Find each parasitized red blood cell.
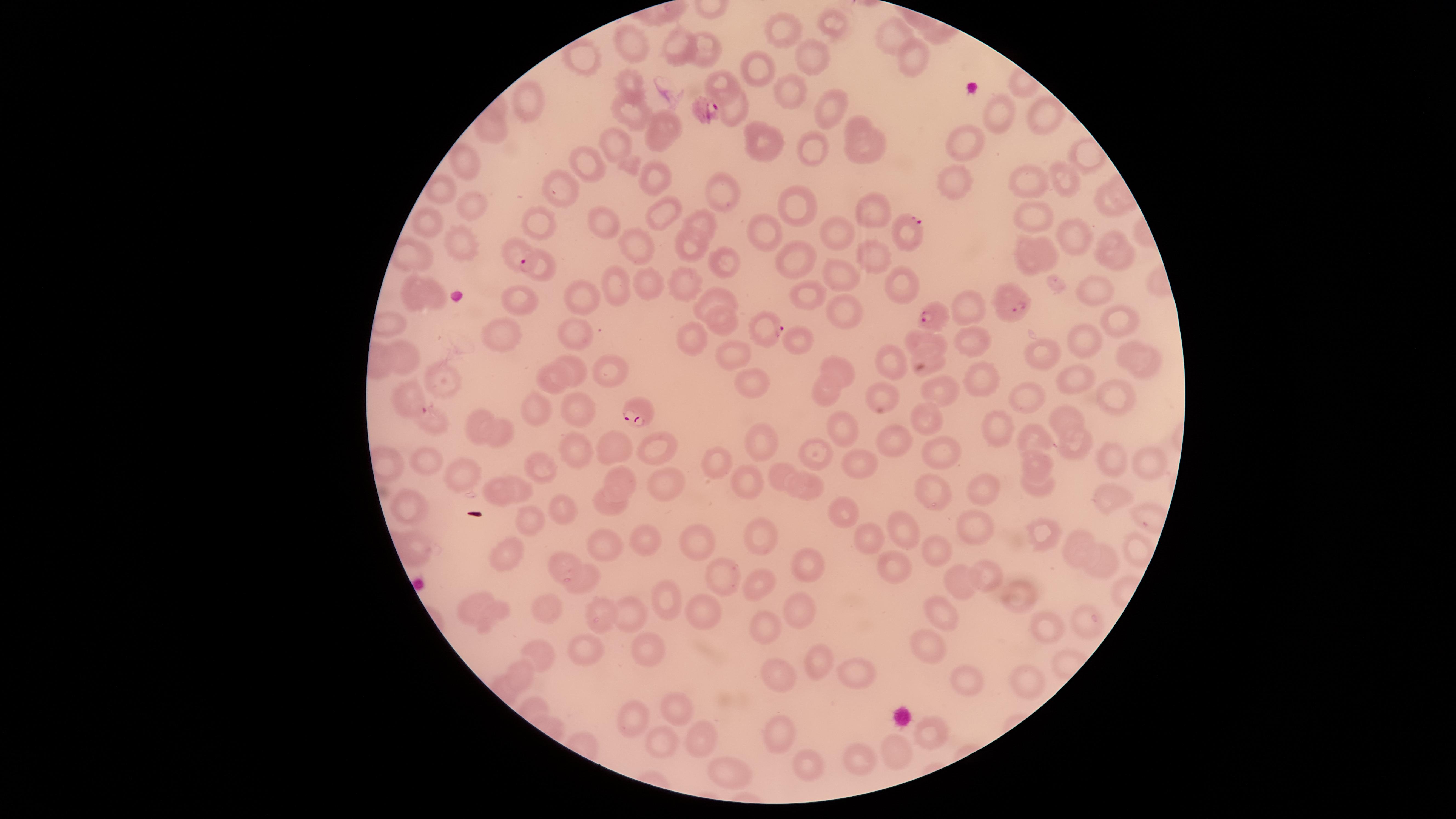
Approximate marker points, in pixels from the top-left corner.
Parasitized red blood cells: (x=705, y=108), (x=913, y=232), (x=521, y=255), (x=1010, y=301), (x=939, y=315), (x=767, y=326), (x=412, y=397), (x=406, y=400), (x=637, y=411).

Approximate marker points, in pixels from the top-left corner. Uninfected red blood cells: (x=791, y=26), (x=837, y=26), (x=893, y=33), (x=680, y=41), (x=707, y=44), (x=631, y=45), (x=813, y=59), (x=587, y=63), (x=908, y=68), (x=753, y=69), (x=718, y=82), (x=628, y=86), (x=784, y=87), (x=529, y=105), (x=823, y=108), (x=999, y=115), (x=1046, y=115), (x=627, y=116), (x=735, y=118), (x=857, y=123), (x=670, y=125), (x=492, y=135), (x=960, y=141), (x=767, y=143), (x=618, y=145), (x=655, y=145), (x=863, y=150), (x=811, y=154), (x=466, y=162), (x=580, y=162), (x=651, y=174), (x=1033, y=181), (x=1067, y=181), (x=947, y=183), (x=441, y=188), (x=560, y=192), (x=719, y=195), (x=791, y=201), (x=473, y=207), (x=880, y=210), (x=1034, y=212), (x=660, y=215), (x=705, y=218), (x=606, y=220), (x=429, y=221), (x=537, y=227), (x=840, y=229), (x=765, y=232), (x=1068, y=235), (x=1046, y=241), (x=459, y=243), (x=637, y=245), (x=690, y=245), (x=1114, y=250), (x=410, y=254), (x=870, y=256), (x=797, y=258), (x=1029, y=261), (x=724, y=267), (x=545, y=272), (x=836, y=274), (x=644, y=275), (x=618, y=284), (x=690, y=284), (x=902, y=287), (x=1094, y=290), (x=805, y=292), (x=414, y=293), (x=432, y=294), (x=587, y=295), (x=714, y=295), (x=517, y=298), (x=836, y=314), (x=1115, y=320), (x=721, y=325), (x=578, y=329), (x=971, y=336), (x=496, y=339), (x=693, y=339), (x=791, y=339), (x=1078, y=341), (x=929, y=342), (x=1044, y=349), (x=1132, y=350), (x=735, y=351), (x=405, y=353), (x=893, y=360), (x=921, y=364), (x=840, y=366), (x=574, y=367), (x=611, y=369), (x=1152, y=369), (x=555, y=377), (x=1071, y=377), (x=980, y=378), (x=441, y=380), (x=753, y=380), (x=824, y=388), (x=943, y=395), (x=1018, y=395), (x=1115, y=395), (x=882, y=398), (x=578, y=409), (x=543, y=412), (x=1068, y=416), (x=924, y=418), (x=432, y=422), (x=1000, y=424), (x=845, y=426), (x=477, y=430), (x=498, y=436), (x=1031, y=436), (x=896, y=440), (x=759, y=447), (x=1070, y=447), (x=615, y=449), (x=661, y=449), (x=575, y=450), (x=816, y=453), (x=941, y=454), (x=1117, y=460), (x=717, y=461), (x=1035, y=462), (x=1148, y=463), (x=428, y=464), (x=854, y=467), (x=541, y=471), (x=777, y=473), (x=749, y=478), (x=464, y=479), (x=623, y=479), (x=665, y=482), (x=811, y=487), (x=520, y=488), (x=934, y=490), (x=981, y=490), (x=495, y=491), (x=1034, y=491), (x=1112, y=498), (x=607, y=505), (x=560, y=507), (x=843, y=511), (x=406, y=514), (x=906, y=522), (x=532, y=523), (x=977, y=526), (x=1045, y=531), (x=757, y=538), (x=864, y=538), (x=694, y=540), (x=643, y=543), (x=605, y=544), (x=415, y=547), (x=942, y=547), (x=1078, y=547), (x=505, y=552), (x=558, y=561), (x=888, y=563), (x=805, y=568), (x=716, y=571), (x=985, y=574), (x=963, y=577), (x=590, y=579), (x=764, y=589), (x=1024, y=590), (x=669, y=595), (x=470, y=606), (x=545, y=612), (x=495, y=613), (x=699, y=613), (x=633, y=614), (x=798, y=614), (x=937, y=614), (x=600, y=615), (x=1048, y=621), (x=1083, y=623), (x=770, y=633), (x=650, y=648), (x=926, y=651), (x=585, y=655), (x=542, y=656), (x=816, y=664), (x=518, y=675), (x=777, y=677), (x=856, y=677), (x=970, y=677), (x=1021, y=680), (x=679, y=706), (x=640, y=711), (x=928, y=728), (x=781, y=736), (x=698, y=739), (x=661, y=740), (x=900, y=748), (x=858, y=752), (x=812, y=768), (x=722, y=771). The visible region is circular. Thin blood film. Giemsa-stained preparation. Image is 1456×819 pixels. Single field of view. Photographed with a smartphone camera through the microscope eyepiece. Species: Plasmodium falciparum.